Locate every Plasmodium ovale-infected red blood cell.
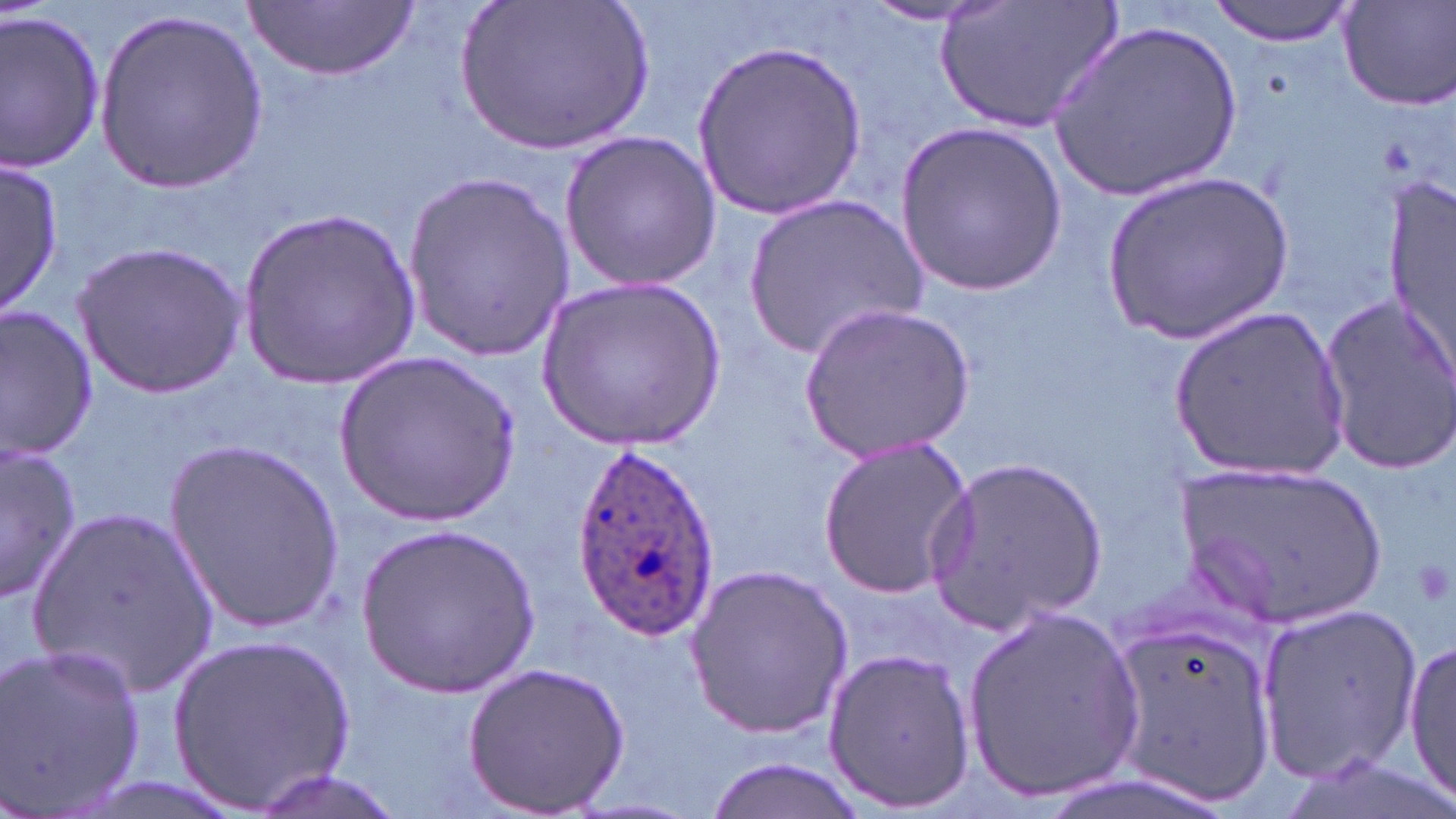

Approximate bounding boxes as named x1/y1/x2/y2 corners in pixels.
Plasmodium ovale-infected red blood cells: (x1=573, y1=442, x2=718, y2=639).

Uninfected red blood cell locations: (x1=452, y1=0, x2=660, y2=156), (x1=935, y1=0, x2=1124, y2=136), (x1=1207, y1=0, x2=1360, y2=46), (x1=245, y1=1, x2=417, y2=81), (x1=853, y1=2, x2=1007, y2=26), (x1=1337, y1=2, x2=1456, y2=111), (x1=94, y1=7, x2=267, y2=193), (x1=0, y1=10, x2=105, y2=170), (x1=1050, y1=18, x2=1245, y2=202), (x1=693, y1=39, x2=865, y2=220), (x1=895, y1=120, x2=1066, y2=298), (x1=558, y1=127, x2=724, y2=295), (x1=1, y1=162, x2=62, y2=316), (x1=1389, y1=166, x2=1454, y2=393), (x1=400, y1=170, x2=572, y2=361), (x1=1098, y1=170, x2=1295, y2=345), (x1=739, y1=193, x2=925, y2=362), (x1=240, y1=205, x2=420, y2=389), (x1=73, y1=242, x2=247, y2=395), (x1=540, y1=276, x2=729, y2=450), (x1=1316, y1=291, x2=1456, y2=476), (x1=798, y1=301, x2=975, y2=460), (x1=0, y1=306, x2=100, y2=458), (x1=1167, y1=306, x2=1352, y2=487), (x1=335, y1=351, x2=521, y2=523), (x1=816, y1=436, x2=977, y2=600), (x1=164, y1=440, x2=344, y2=631), (x1=1, y1=441, x2=83, y2=604), (x1=927, y1=453, x2=1107, y2=637), (x1=1173, y1=462, x2=1388, y2=631), (x1=28, y1=506, x2=219, y2=697), (x1=353, y1=522, x2=545, y2=702), (x1=685, y1=562, x2=854, y2=739), (x1=1254, y1=603, x2=1422, y2=784), (x1=959, y1=605, x2=1146, y2=805), (x1=1105, y1=612, x2=1281, y2=809), (x1=166, y1=634, x2=355, y2=815), (x1=1405, y1=635, x2=1456, y2=808), (x1=1, y1=641, x2=149, y2=816), (x1=822, y1=643, x2=977, y2=812), (x1=462, y1=660, x2=631, y2=816), (x1=697, y1=757, x2=875, y2=818), (x1=246, y1=770, x2=407, y2=819). Platelet locations: (x1=1410, y1=555, x2=1453, y2=610). Slide-level diagnosis: Plasmodium ovale. May-Grünwald-Giemsa-stained preparation. Optical microscopy. 1000x magnification. Single field of view. Thin blood smear. Image is 1456×819 pixels.